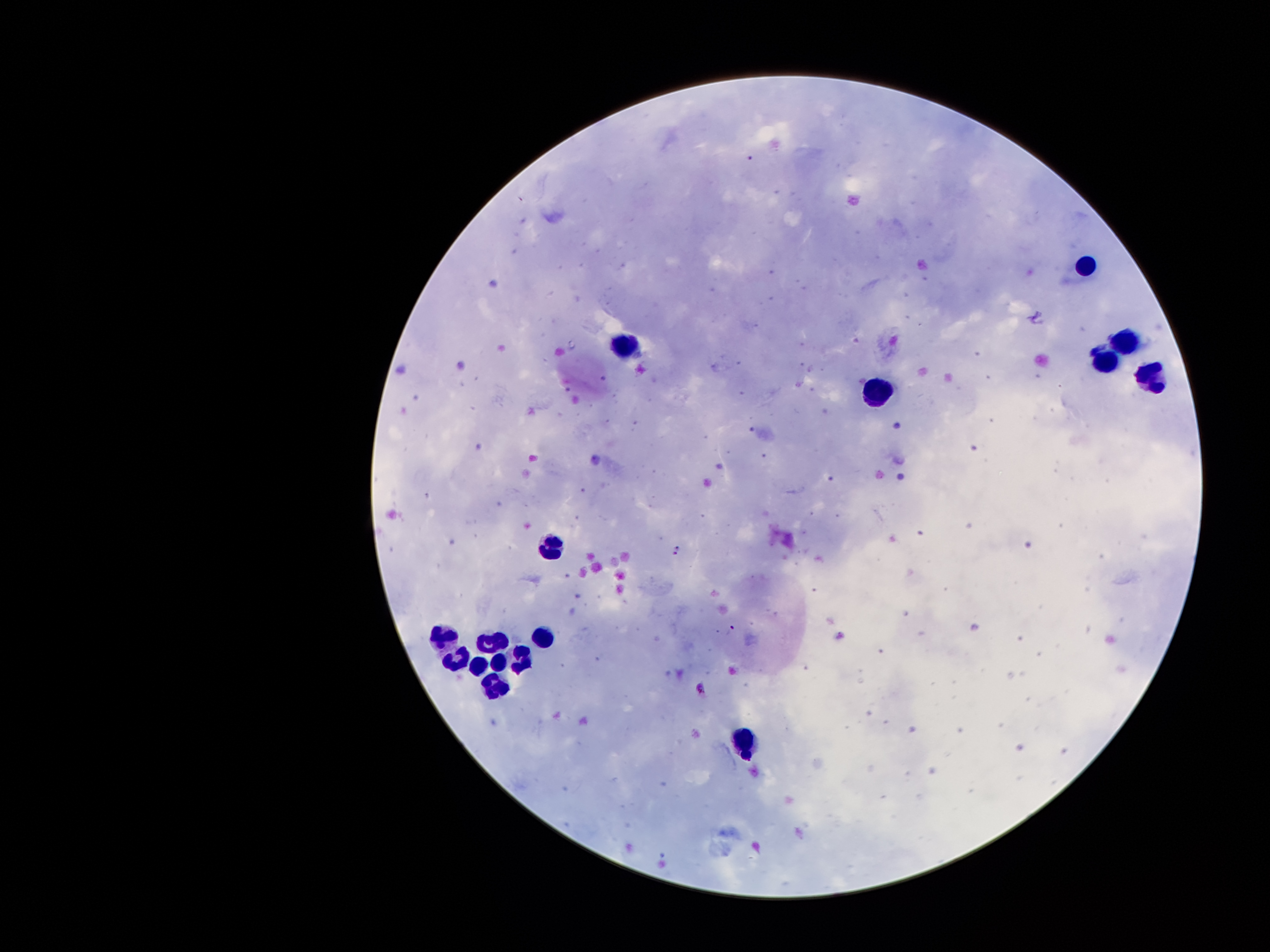
field_of_view: one from this slide
patient_malaria_status: positive for Plasmodium falciparum
preparation: thick peripheral-blood smear
leukocyte_locations: 'approximate object centers, in pixels from the top-left corner: (x=1085, y=263), (x=1124, y=341), (x=625, y=344), (x=1099, y=358), (x=1150, y=374), (x=882, y=392), (x=550, y=553), (x=503, y=635), (x=543, y=637), (x=445, y=639), (x=483, y=642), (x=520, y=658), (x=460, y=663), (x=495, y=664), (x=477, y=670), (x=494, y=684), (x=744, y=742)'
magnification: 100x
capture: smartphone camera through the microscope eyepiece
stain: Giemsa
malaria_parasite_locations: 'approximate object centers, in pixels from the top-left corner: (x=749, y=158), (x=597, y=461), (x=678, y=549), (x=733, y=627), (x=702, y=688)'
image_size: 1270×952 pixels